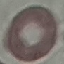
Summary:
  - Result: no malaria parasites seen
  - Preparation: thin blood smear
  - Image type: automatically extracted cell patch, resized to 64 × 64 pixels
  - Stain: Giemsa
  - Capture: smartphone through the microscope eyepiece